Assess the morphology of the erythrocytes.
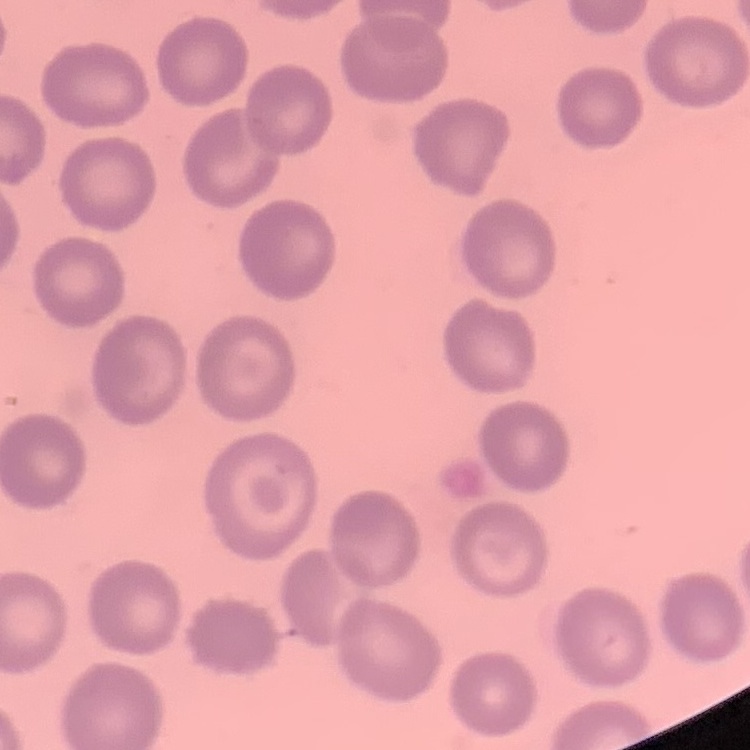
They show no rouleaux formation.

Summary:
  - Stain: Field's or Giemsa
  - Preparation: thin blood film
  - Image type: one tile cut from a larger photomicrograph